State which cell type is depicted.
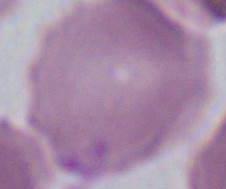
This is an erythrocyte.

{
  "modality": "photomicrograph",
  "magnification": "1000x"
}